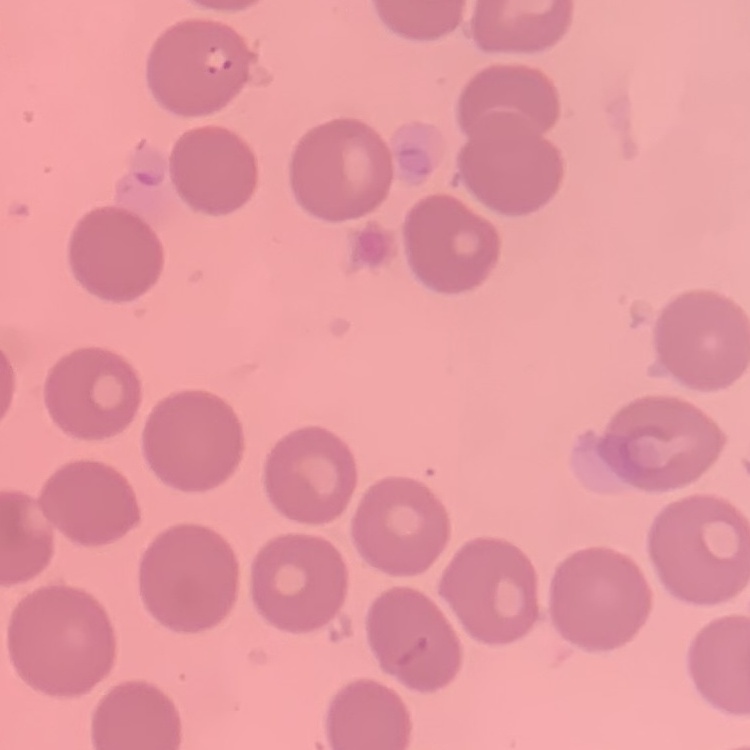

The red blood cells show no rouleaux formation. Thin peripheral smear. Field's or Giemsa stain. Square crop of a larger photomicrograph.